Locate every Plasmodium parasite.
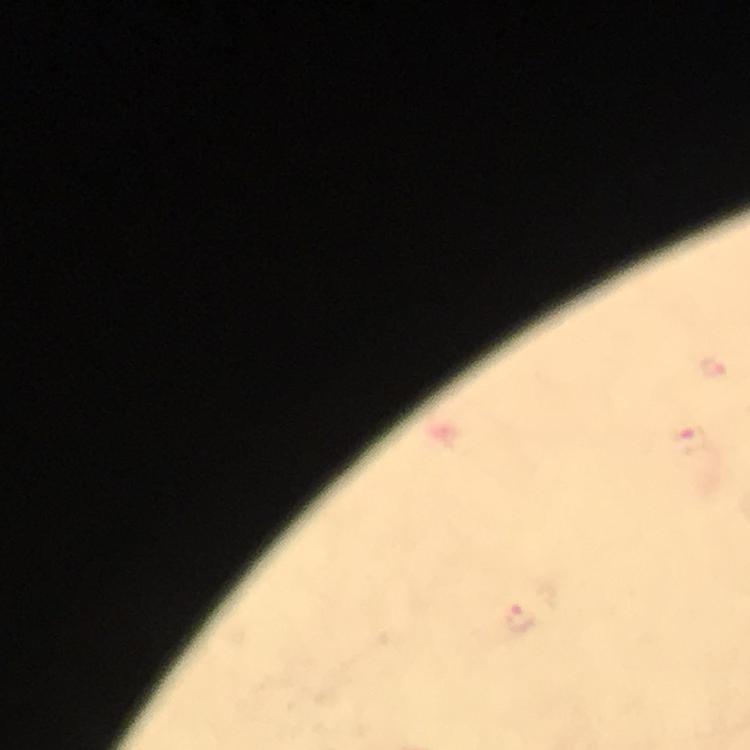
Approximate object centers, in pixels from the top-left corner.
Plasmodium parasites: (x=716, y=369), (x=689, y=440), (x=518, y=615).

cropped_from: one field of view
image_size: 750×750 pixels
capture: smartphone camera through the microscope
preparation: thick smear
context: from a malaria diagnostic workup
stain: Giemsa
immersion_oil: applied
magnification: 100x